Report the malaria status of this cell.
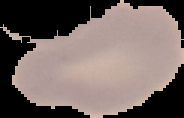

It is uninfected.

preparation = thin blood smear
image type = segmented cell region on a black background
image size = 184×118 pixels